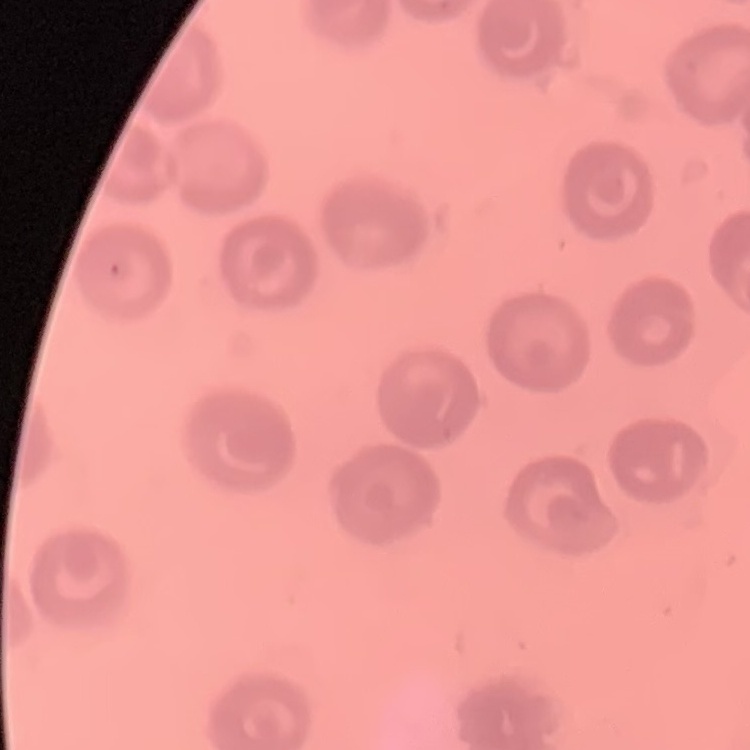

Summary:
  - Red blood cell morphology: no rouleaux formation
  - Image type: one tile cut from a larger photomicrograph
  - Stain: Field's or Giemsa
  - Preparation: thin blood film